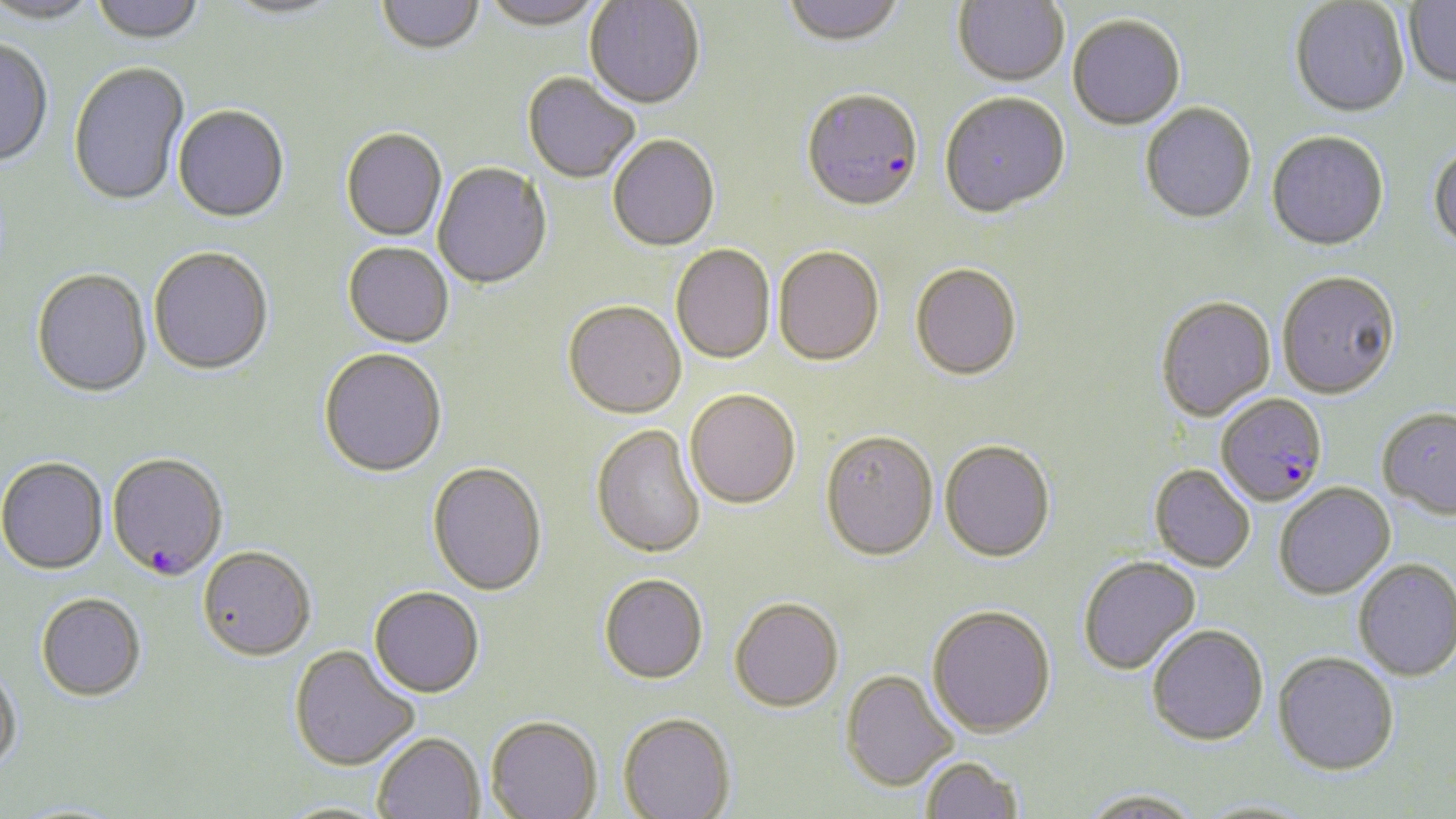
Summary:
  - Coordinate format: approximate bounding boxes as named x1/y1/x2/y2 corners in pixels
  - Plasmodium falciparum-infected red blood cell locations: (x1=802, y1=93, x2=923, y2=215), (x1=1216, y1=394, x2=1328, y2=507), (x1=106, y1=455, x2=228, y2=583)
  - Uninfected red blood cell locations: (x1=0, y1=0, x2=101, y2=28), (x1=89, y1=0, x2=206, y2=47), (x1=376, y1=0, x2=484, y2=57), (x1=479, y1=0, x2=604, y2=34), (x1=585, y1=0, x2=704, y2=111), (x1=781, y1=0, x2=907, y2=51), (x1=953, y1=0, x2=1070, y2=89), (x1=219, y1=1, x2=348, y2=23), (x1=1289, y1=1, x2=1410, y2=119), (x1=1404, y1=1, x2=1456, y2=90), (x1=1067, y1=17, x2=1186, y2=132), (x1=0, y1=41, x2=53, y2=170), (x1=68, y1=63, x2=190, y2=209), (x1=522, y1=74, x2=639, y2=185), (x1=940, y1=95, x2=1070, y2=220), (x1=1140, y1=104, x2=1257, y2=226), (x1=172, y1=107, x2=289, y2=225), (x1=341, y1=130, x2=447, y2=242), (x1=1266, y1=132, x2=1389, y2=252), (x1=608, y1=137, x2=720, y2=254), (x1=1428, y1=143, x2=1456, y2=253), (x1=432, y1=164, x2=552, y2=291), (x1=343, y1=244, x2=454, y2=349), (x1=671, y1=246, x2=775, y2=366), (x1=773, y1=248, x2=884, y2=368), (x1=149, y1=249, x2=274, y2=378), (x1=910, y1=265, x2=1022, y2=383), (x1=31, y1=271, x2=152, y2=400), (x1=1277, y1=272, x2=1401, y2=400), (x1=1156, y1=297, x2=1276, y2=423), (x1=562, y1=303, x2=686, y2=421), (x1=318, y1=350, x2=447, y2=480), (x1=685, y1=391, x2=801, y2=511), (x1=1377, y1=407, x2=1456, y2=518), (x1=591, y1=425, x2=706, y2=560), (x1=820, y1=433, x2=939, y2=562), (x1=939, y1=442, x2=1055, y2=564), (x1=0, y1=459, x2=108, y2=576), (x1=427, y1=463, x2=547, y2=598), (x1=1149, y1=465, x2=1256, y2=573), (x1=1274, y1=482, x2=1396, y2=599), (x1=198, y1=549, x2=316, y2=663), (x1=1078, y1=556, x2=1201, y2=675), (x1=1354, y1=558, x2=1455, y2=682), (x1=599, y1=575, x2=708, y2=686), (x1=369, y1=589, x2=484, y2=700), (x1=35, y1=595, x2=146, y2=703), (x1=729, y1=598, x2=843, y2=713), (x1=927, y1=605, x2=1056, y2=736), (x1=1146, y1=624, x2=1269, y2=745), (x1=289, y1=645, x2=419, y2=772), (x1=1272, y1=651, x2=1399, y2=775), (x1=0, y1=665, x2=23, y2=777), (x1=840, y1=670, x2=958, y2=791), (x1=618, y1=714, x2=736, y2=819), (x1=486, y1=717, x2=603, y2=819), (x1=372, y1=733, x2=485, y2=819), (x1=920, y1=756, x2=1024, y2=818), (x1=1078, y1=788, x2=1205, y2=819)
  - Slide-level diagnosis: Plasmodium falciparum
  - Modality: light microscopy
  - Stain: May-Grünwald-Giemsa
  - Field of view: single
  - Magnification: 1000x
  - Image size: 1456×819 pixels
  - Preparation: thin blood smear